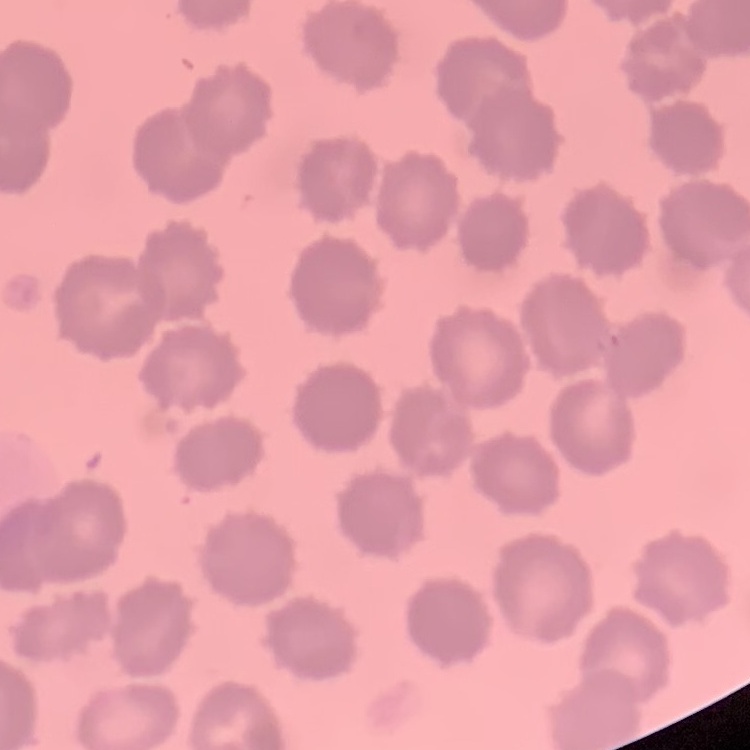

Summary:
  - Erythrocyte morphology: no rouleaux formation
  - Image type: square crop of a larger photomicrograph
  - Stain: Field's or Giemsa
  - Preparation: thin blood smear